State the blood parasite species.
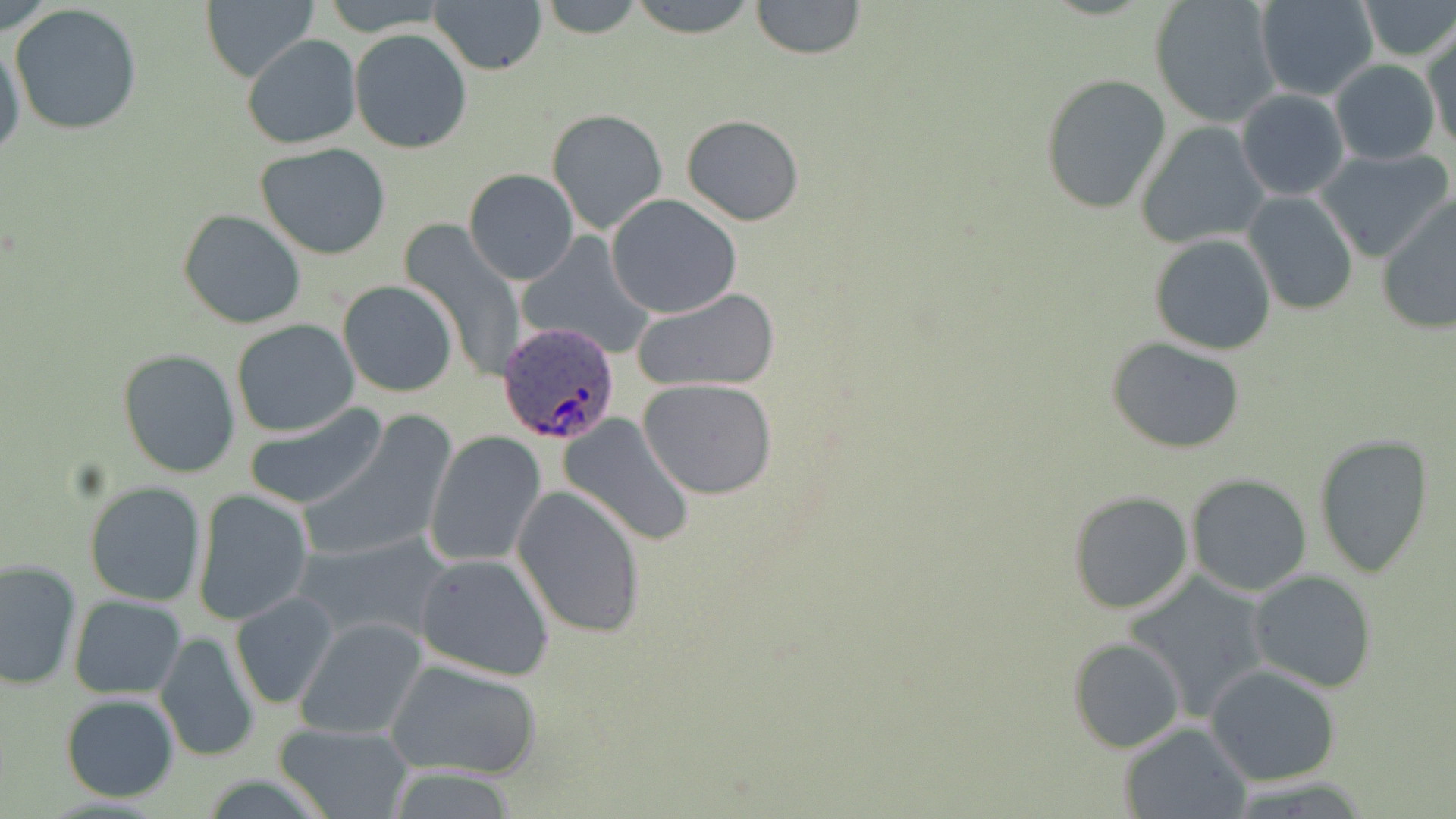

Plasmodium ovale.

Summary:
  - Coordinate format: approximate bounding boxes as named x1/y1/x2/y2 corners in pixels
  - Uninfected red blood cell locations: (x1=535, y1=0, x2=648, y2=39), (x1=624, y1=0, x2=761, y2=38), (x1=749, y1=0, x2=867, y2=61), (x1=1150, y1=0, x2=1281, y2=127), (x1=1256, y1=0, x2=1379, y2=101), (x1=1356, y1=0, x2=1455, y2=61), (x1=431, y1=1, x2=547, y2=76), (x1=203, y1=2, x2=316, y2=83), (x1=9, y1=3, x2=145, y2=137), (x1=350, y1=28, x2=471, y2=154), (x1=1422, y1=29, x2=1456, y2=150), (x1=1, y1=32, x2=26, y2=166), (x1=241, y1=34, x2=361, y2=150), (x1=1330, y1=59, x2=1440, y2=166), (x1=1040, y1=73, x2=1172, y2=216), (x1=1236, y1=88, x2=1351, y2=201), (x1=547, y1=108, x2=669, y2=234), (x1=680, y1=114, x2=805, y2=225), (x1=1135, y1=120, x2=1268, y2=249), (x1=256, y1=144, x2=392, y2=260), (x1=1315, y1=146, x2=1453, y2=262), (x1=464, y1=168, x2=579, y2=285), (x1=1244, y1=190, x2=1360, y2=315), (x1=1377, y1=193, x2=1456, y2=336), (x1=608, y1=194, x2=743, y2=318), (x1=178, y1=209, x2=307, y2=329), (x1=397, y1=220, x2=526, y2=384), (x1=516, y1=232, x2=653, y2=357), (x1=1149, y1=234, x2=1276, y2=355), (x1=338, y1=280, x2=458, y2=398), (x1=631, y1=288, x2=780, y2=394), (x1=231, y1=319, x2=361, y2=437), (x1=1107, y1=338, x2=1246, y2=453), (x1=118, y1=348, x2=241, y2=478), (x1=639, y1=380, x2=779, y2=499), (x1=241, y1=403, x2=389, y2=511), (x1=557, y1=412, x2=696, y2=547), (x1=301, y1=417, x2=456, y2=564), (x1=423, y1=431, x2=545, y2=567), (x1=1311, y1=432, x2=1435, y2=578), (x1=1187, y1=473, x2=1314, y2=594), (x1=84, y1=480, x2=206, y2=607), (x1=513, y1=485, x2=644, y2=638), (x1=192, y1=488, x2=315, y2=624), (x1=1067, y1=489, x2=1194, y2=614), (x1=292, y1=528, x2=455, y2=650), (x1=414, y1=552, x2=557, y2=680), (x1=1, y1=558, x2=83, y2=690), (x1=1249, y1=570, x2=1378, y2=693), (x1=1123, y1=571, x2=1273, y2=722), (x1=229, y1=591, x2=339, y2=710), (x1=69, y1=594, x2=187, y2=699), (x1=293, y1=617, x2=428, y2=740), (x1=154, y1=629, x2=260, y2=763), (x1=1068, y1=636, x2=1185, y2=754), (x1=385, y1=659, x2=542, y2=781), (x1=1205, y1=664, x2=1343, y2=786), (x1=59, y1=692, x2=180, y2=803), (x1=1119, y1=721, x2=1251, y2=819), (x1=276, y1=723, x2=414, y2=818)
  - Plasmodium ovale-infected red blood cell locations: (x1=498, y1=326, x2=620, y2=444)
  - Stain: May-Grünwald-Giemsa
  - Magnification: 1000x
  - Preparation: thin blood film
  - Field of view: single
  - Image size: 1456×819 pixels
  - Modality: light microscopy